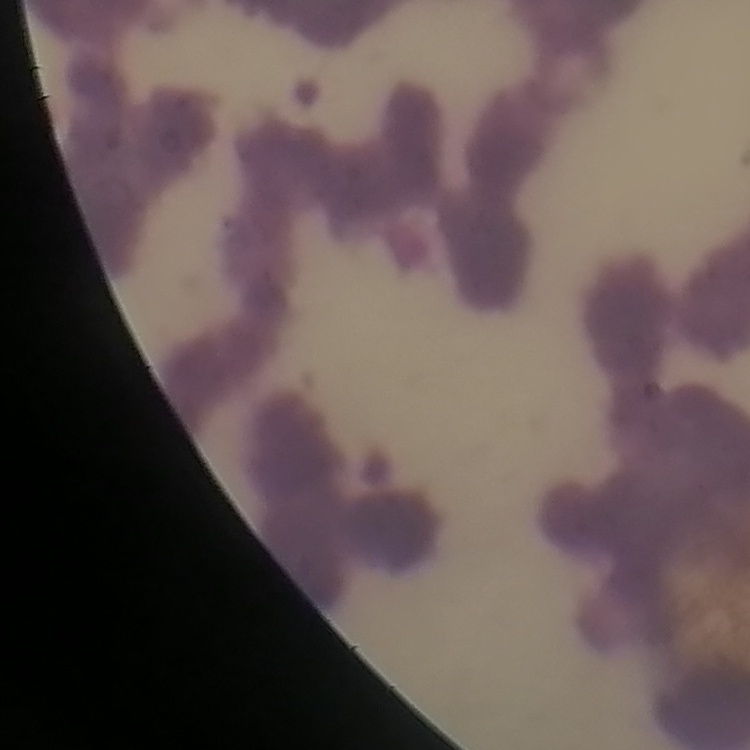
Summary:
  - Red blood cell morphology: rouleaux formation
  - Image type: one tile cut from a larger photomicrograph
  - Preparation: thin peripheral smear
  - Stain: Field's or Giemsa